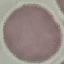
{
  "result": "no malaria parasites detected",
  "capture": "smartphone camera at the microscope eyepiece",
  "preparation": "thin smear",
  "stain": "Giemsa",
  "image_type": "automatically extracted cell patch, resized to 64 × 64 pixels"
}